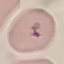

Summary:
  - Result: malaria parasites detected
  - Preparation: thin smear
  - Stain: Giemsa
  - Capture: smartphone camera at the microscope eyepiece
  - Image type: cell patch, automatically extracted from a larger field of view and resized to 64 × 64 pixels